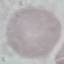

result: negative for malaria parasites
image_type: cell patch, automatically extracted from a larger field of view and resized to 64 × 64 pixels
capture: smartphone camera at the microscope eyepiece
stain: Giemsa
preparation: thin blood smear